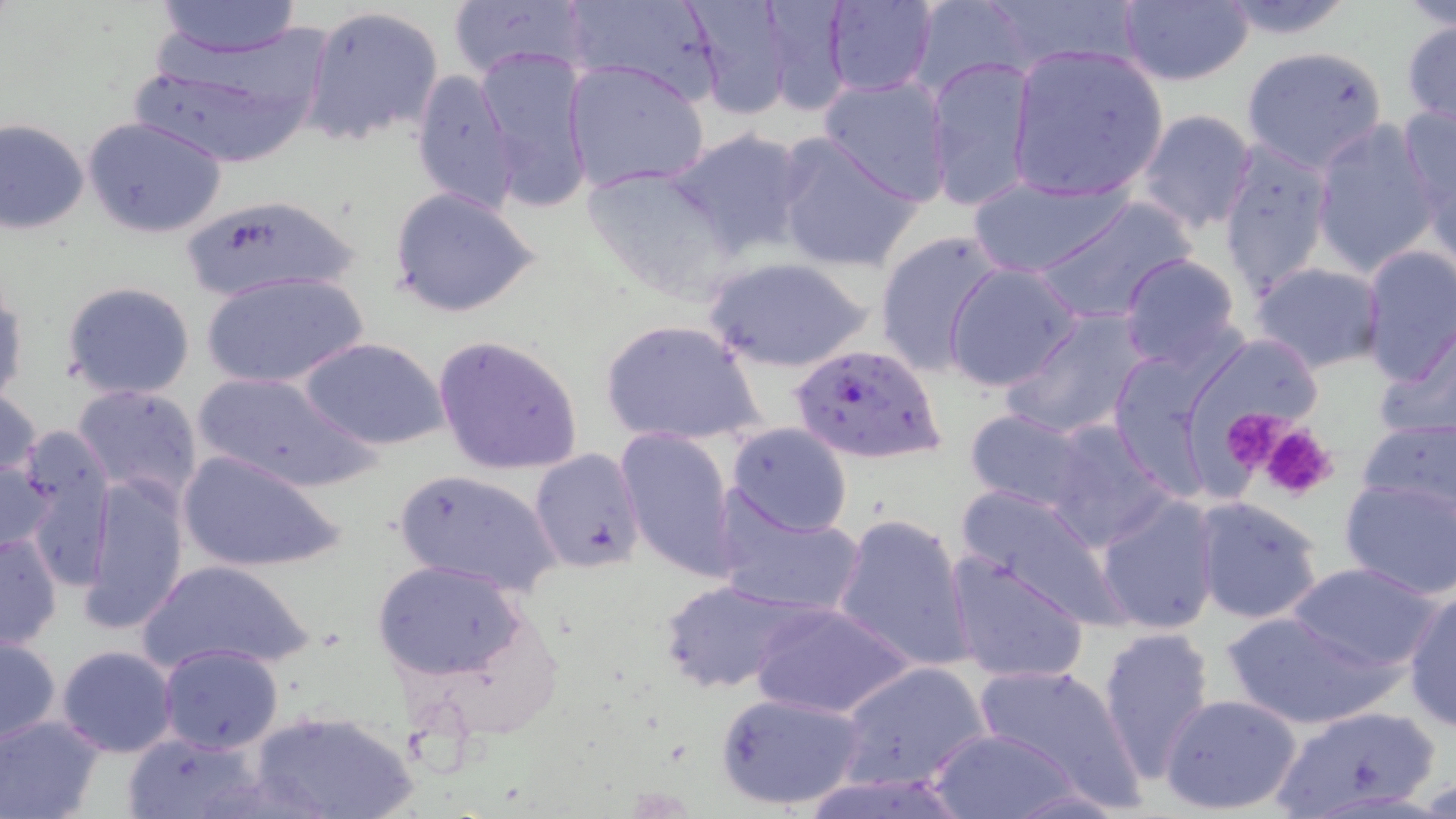

{
  "plasmodium_falciparum_infected_red_blood_cell_locations": "approximate bounding boxes as named x1/y1/x2/y2 corners in pixels: (x1=787, y1=341, x2=944, y2=466)",
  "slide_level_diagnosis": "Plasmodium falciparum",
  "magnification": "1000x",
  "uninfected_red_blood_cell_locations": "approximate bounding boxes as named x1/y1/x2/y2 corners in pixels: (x1=143, y1=0, x2=319, y2=116), (x1=563, y1=0, x2=726, y2=104), (x1=683, y1=0, x2=797, y2=122), (x1=754, y1=0, x2=854, y2=118), (x1=823, y1=0, x2=937, y2=96), (x1=910, y1=0, x2=1032, y2=97), (x1=1217, y1=0, x2=1358, y2=39), (x1=153, y1=1, x2=302, y2=58), (x1=447, y1=1, x2=593, y2=82), (x1=1117, y1=1, x2=1253, y2=87), (x1=301, y1=4, x2=446, y2=148), (x1=1401, y1=19, x2=1456, y2=128), (x1=131, y1=36, x2=328, y2=169), (x1=1006, y1=44, x2=1168, y2=201), (x1=475, y1=46, x2=596, y2=213), (x1=1239, y1=46, x2=1391, y2=172), (x1=925, y1=54, x2=1038, y2=212), (x1=563, y1=58, x2=712, y2=194), (x1=409, y1=67, x2=521, y2=218), (x1=817, y1=74, x2=952, y2=204), (x1=1396, y1=104, x2=1456, y2=239), (x1=1136, y1=108, x2=1258, y2=233), (x1=83, y1=116, x2=227, y2=238), (x1=1, y1=118, x2=90, y2=235), (x1=1309, y1=121, x2=1441, y2=275), (x1=666, y1=126, x2=812, y2=260), (x1=771, y1=132, x2=924, y2=273), (x1=1217, y1=139, x2=1333, y2=298), (x1=581, y1=163, x2=739, y2=300), (x1=965, y1=172, x2=1137, y2=277), (x1=387, y1=185, x2=544, y2=319), (x1=177, y1=196, x2=362, y2=301), (x1=1032, y1=196, x2=1201, y2=325), (x1=872, y1=230, x2=1007, y2=375), (x1=1358, y1=245, x2=1455, y2=388), (x1=1119, y1=253, x2=1243, y2=371), (x1=700, y1=255, x2=874, y2=373), (x1=1250, y1=262, x2=1386, y2=374), (x1=943, y1=263, x2=1084, y2=392), (x1=202, y1=270, x2=367, y2=390), (x1=61, y1=280, x2=196, y2=399), (x1=0, y1=281, x2=27, y2=408), (x1=1002, y1=310, x2=1152, y2=440), (x1=600, y1=317, x2=766, y2=449), (x1=1371, y1=326, x2=1456, y2=448), (x1=1196, y1=332, x2=1328, y2=434), (x1=432, y1=333, x2=585, y2=477), (x1=298, y1=336, x2=450, y2=452), (x1=191, y1=371, x2=377, y2=493), (x1=71, y1=382, x2=203, y2=502), (x1=0, y1=384, x2=43, y2=494), (x1=962, y1=408, x2=1095, y2=515), (x1=1354, y1=415, x2=1456, y2=520), (x1=1041, y1=418, x2=1174, y2=549), (x1=725, y1=422, x2=854, y2=538), (x1=616, y1=428, x2=738, y2=581), (x1=7, y1=430, x2=115, y2=574), (x1=531, y1=448, x2=650, y2=573), (x1=177, y1=449, x2=347, y2=573), (x1=0, y1=456, x2=57, y2=557), (x1=392, y1=468, x2=561, y2=598), (x1=81, y1=472, x2=191, y2=634), (x1=1338, y1=477, x2=1456, y2=601), (x1=953, y1=485, x2=1126, y2=623), (x1=713, y1=494, x2=864, y2=619), (x1=1095, y1=495, x2=1222, y2=635), (x1=1191, y1=496, x2=1326, y2=625), (x1=831, y1=511, x2=975, y2=673), (x1=0, y1=530, x2=63, y2=650), (x1=944, y1=549, x2=1091, y2=686), (x1=137, y1=559, x2=316, y2=678), (x1=373, y1=560, x2=526, y2=681), (x1=1287, y1=562, x2=1443, y2=672), (x1=657, y1=579, x2=808, y2=695), (x1=1402, y1=586, x2=1456, y2=733), (x1=746, y1=598, x2=916, y2=719), (x1=1222, y1=608, x2=1395, y2=730), (x1=1096, y1=625, x2=1218, y2=781), (x1=1, y1=633, x2=61, y2=746), (x1=157, y1=643, x2=285, y2=754), (x1=55, y1=644, x2=180, y2=757), (x1=836, y1=660, x2=989, y2=790), (x1=973, y1=662, x2=1144, y2=806), (x1=715, y1=692, x2=865, y2=812), (x1=1158, y1=692, x2=1303, y2=817), (x1=1267, y1=703, x2=1445, y2=819), (x1=251, y1=709, x2=418, y2=819), (x1=0, y1=713, x2=104, y2=819), (x1=923, y1=726, x2=1091, y2=817), (x1=122, y1=732, x2=264, y2=819)",
  "preparation": "thin blood film",
  "modality": "light microscopy",
  "stain": "May-Grünwald-Giemsa",
  "platelet_locations": "approximate bounding boxes as named x1/y1/x2/y2 corners in pixels: (x1=1219, y1=407, x2=1304, y2=486), (x1=1257, y1=420, x2=1340, y2=501)",
  "image_size": "1456×819 pixels",
  "field_of_view": "one of a larger specimen"
}